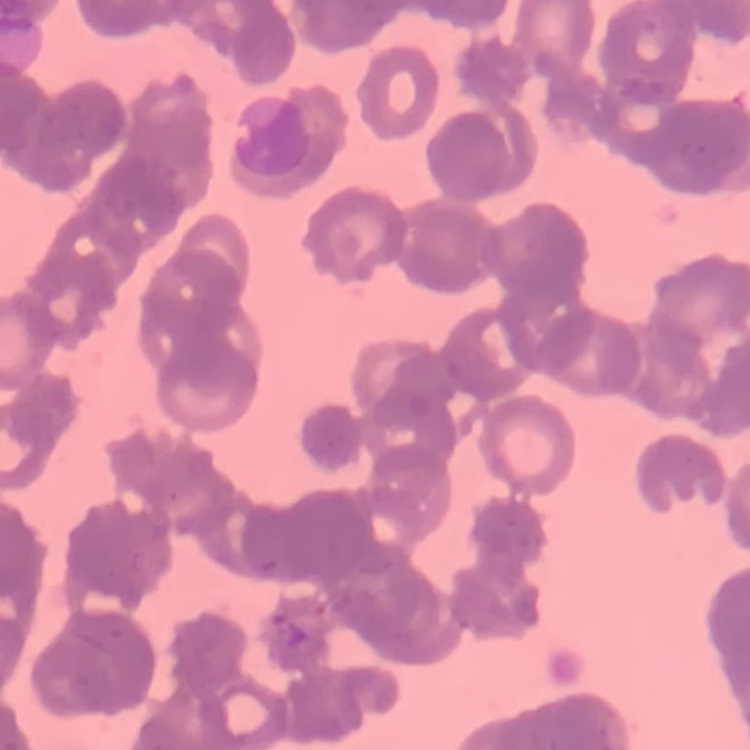
Summary:
  - Erythrocyte morphology: rouleaux formation
  - Preparation: thin peripheral smear
  - Image type: one tile cut from a larger photomicrograph
  - Stain: Field's or Giemsa